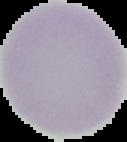

Image is 127×142 pixels. Cell region segmented out of the field of view; the surrounding area is masked to black. Result: no malaria parasites seen. From a thin blood film.